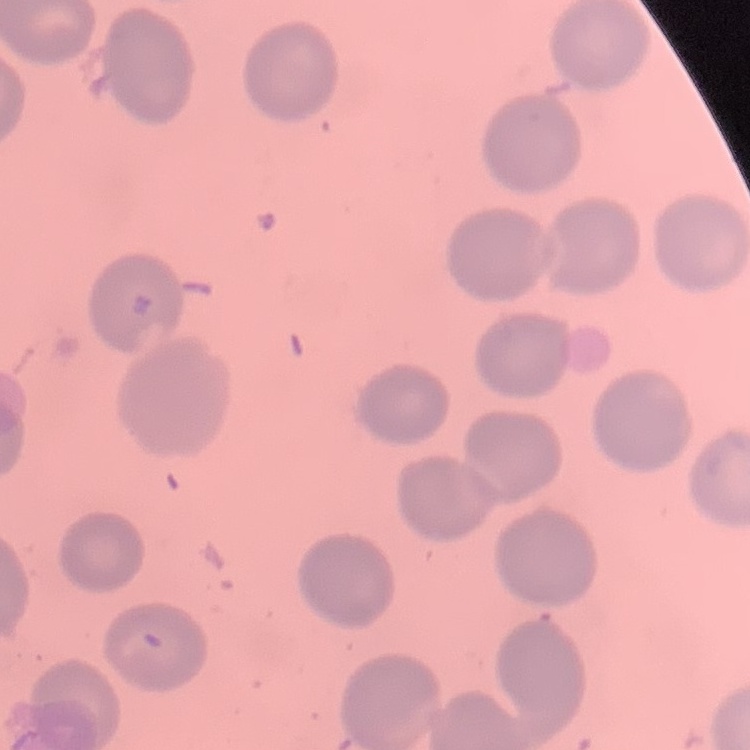

The erythrocytes exhibit no rouleaux formation. Field's or Giemsa stain. Thin blood film. One tile cut from a larger photomicrograph.